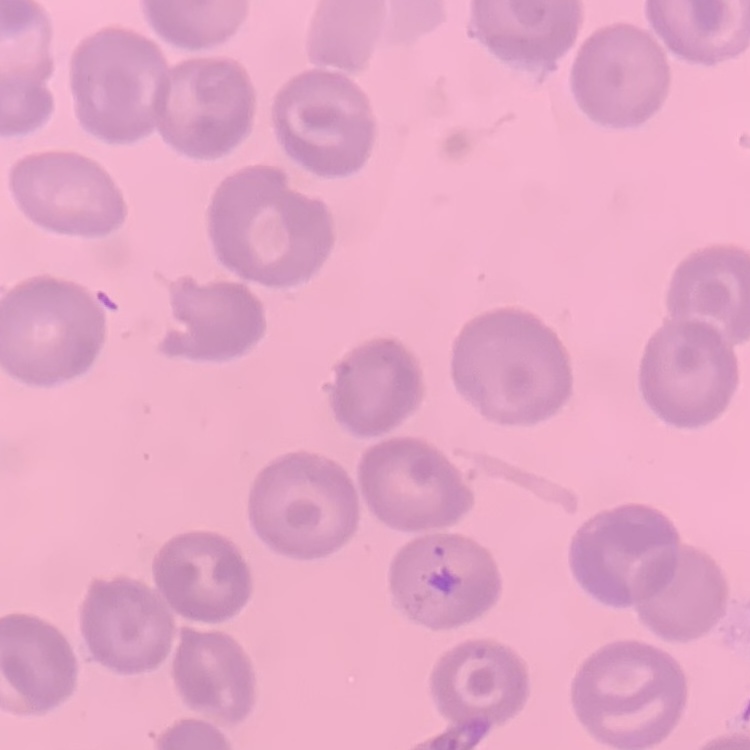 The red blood cells show no rouleaux formation. Square crop of a larger photomicrograph. Thin peripheral smear. Stained with either Field's or Giemsa.